State which parasite is depicted.
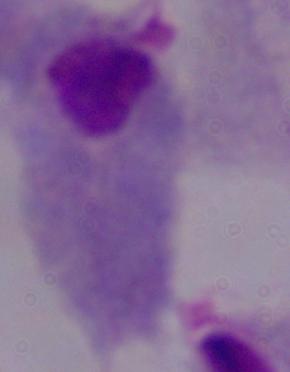

This is a trichomonad.

modality: micrograph
magnification: 1000x